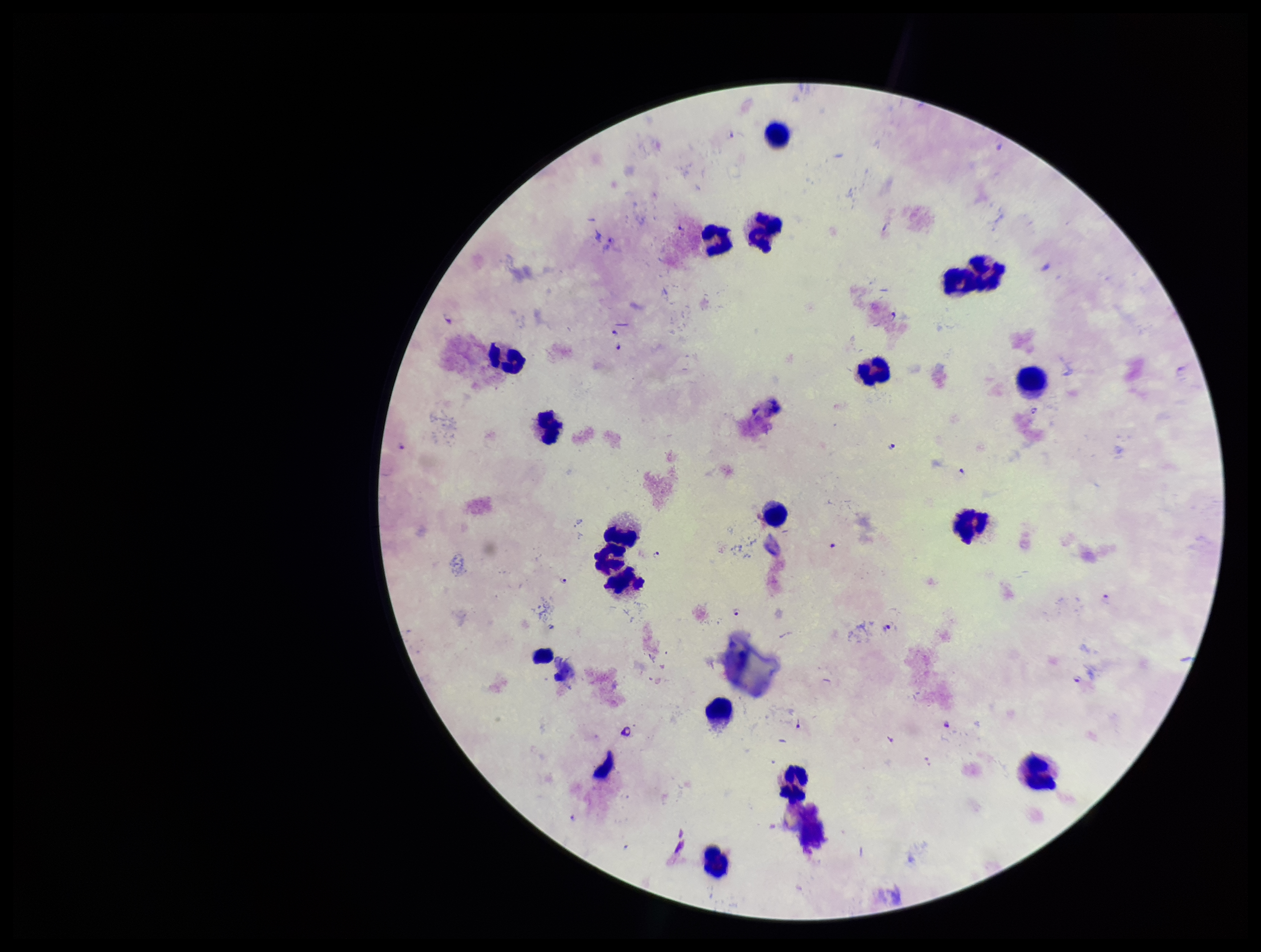
parasite count = 9
stain = Giemsa
capture = smartphone photograph through the microscope eyepiece
field of view = one from this slide
preparation = thick smear
Plasmodium parasites = identified
leukocyte count = 19
species reported for this patient = Plasmodium falciparum
patient malaria status = positive
image size = 1261×952 pixels